Assess the morphology of the erythrocytes.
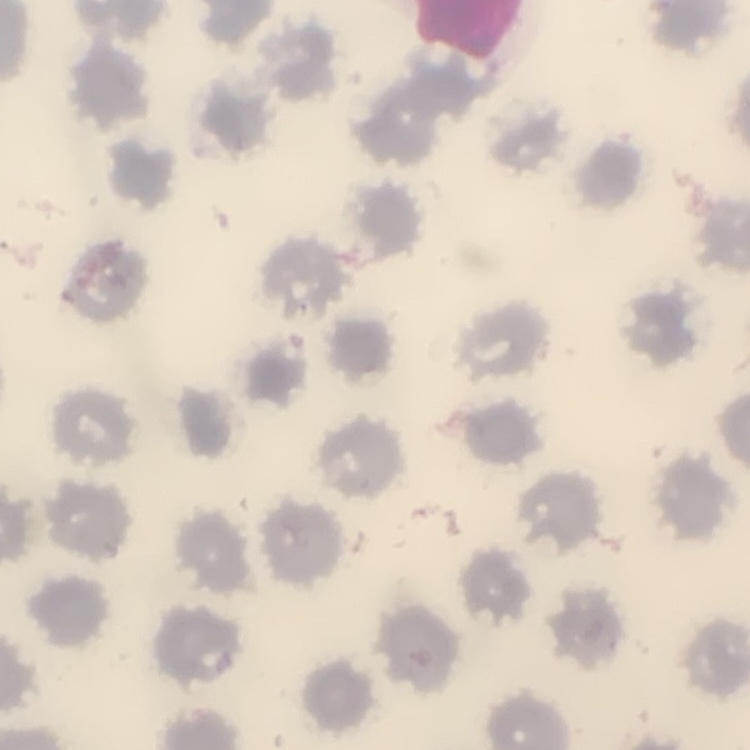
They show no rouleaux formation.

Thin peripheral smear. One tile cut from a larger photomicrograph. Field's or Giemsa stain.